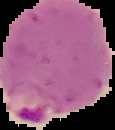

Summary:
  - Image type: cell region segmented out of the field of view; surrounding area masked to black
  - Malaria status: parasitized
  - Image size: 115×130 pixels
  - Preparation: thin blood smear